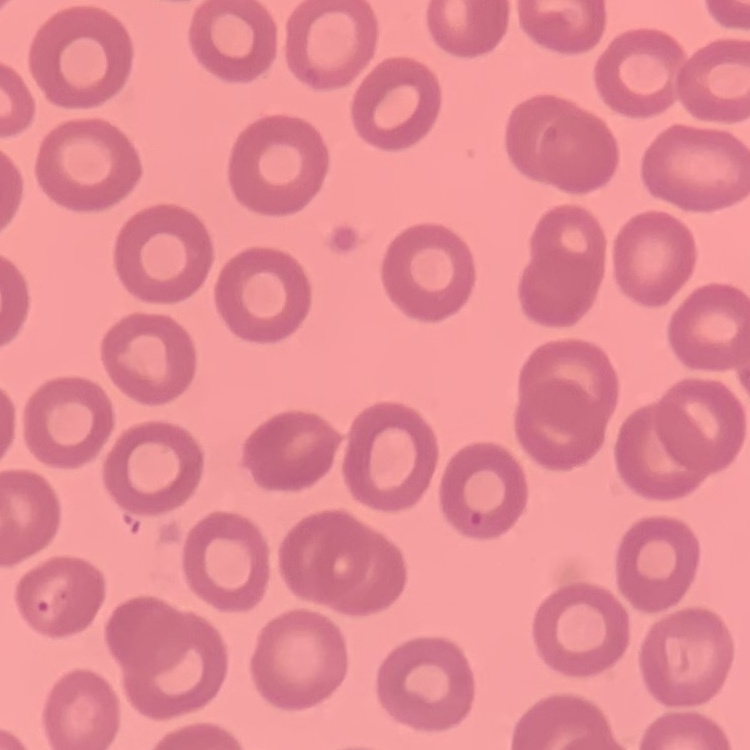
The red blood cells exhibit no rouleaux formation. One tile cut from a larger photomicrograph. Field's or Giemsa stain. Thin peripheral smear.